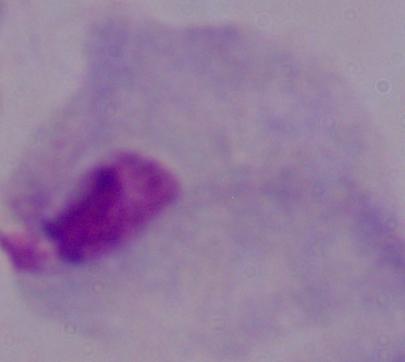

A trichomonad is shown. 1000x magnification. Micrograph.